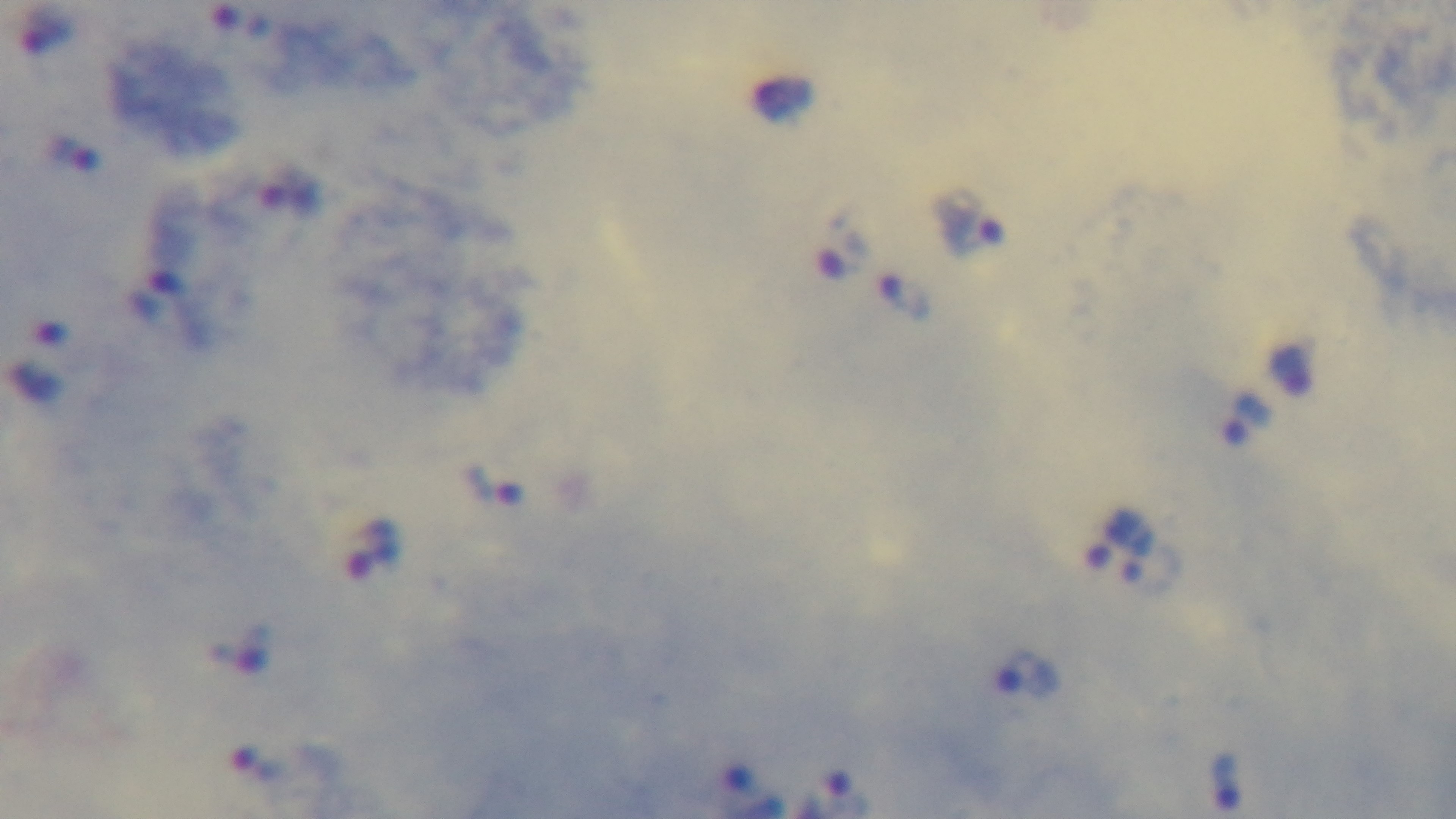

Light microscopy. One field from the slide. Preparation: thick blood film. Mounted 4K digital camera. Malaria status: infected. Giemsa-stained. Oil-immersion objective, 100x.